Assess this cell for malaria.
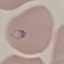
It is parasitized.

{
  "preparation": "thin blood film",
  "image_type": "cell patch, automatically extracted from a larger field of view and resized to 64 × 64 pixels",
  "capture": "smartphone camera at the microscope eyepiece",
  "stain": "Giemsa"
}